Give the extent of all Plasmodium falciparum-infected red blood cells.
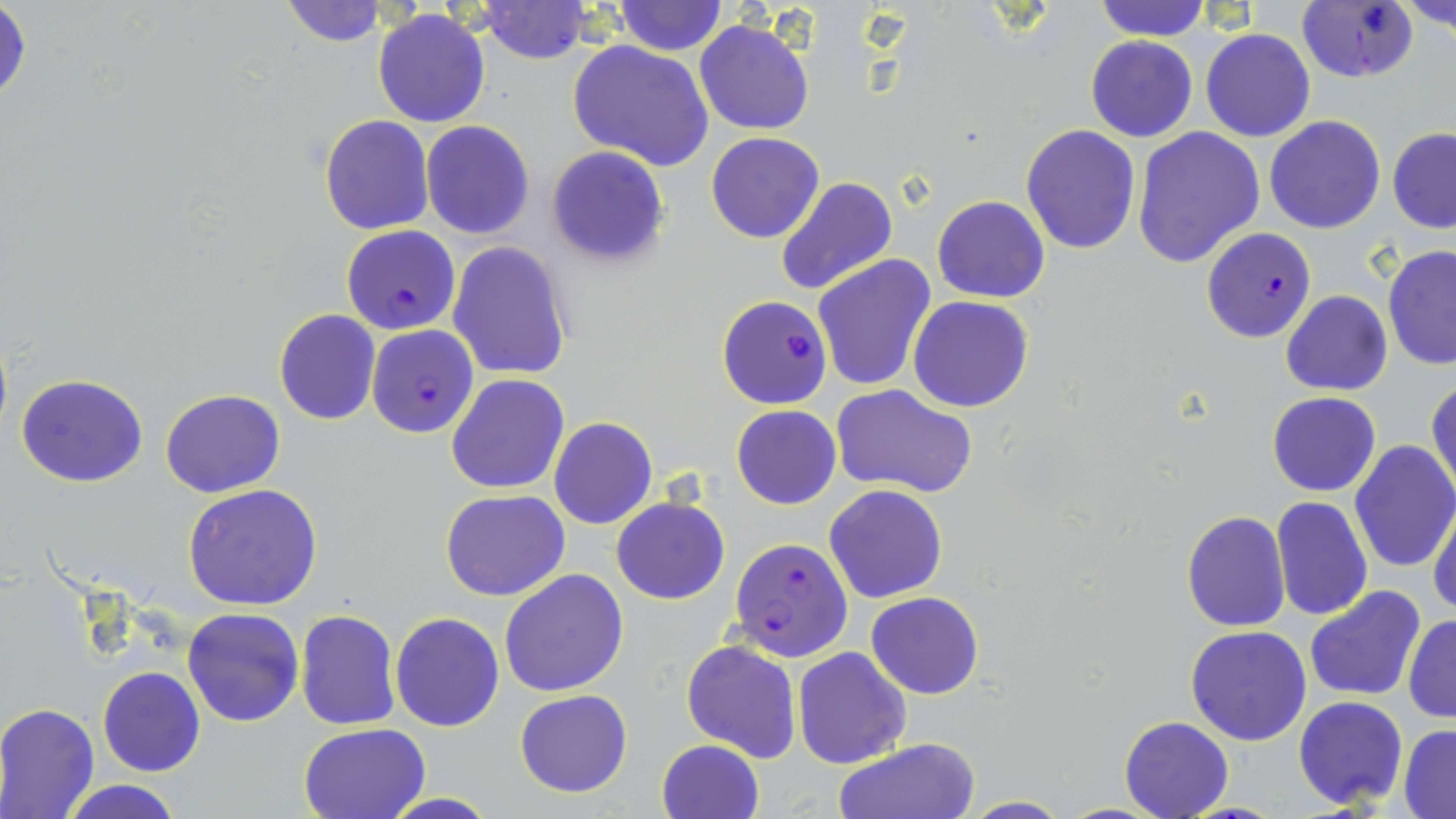
Approximate bounding boxes as named x1/y1/x2/y2 corners in pixels.
Plasmodium falciparum-infected red blood cells: (x1=1294, y1=1, x2=1419, y2=84), (x1=340, y1=225, x2=461, y2=335), (x1=1202, y1=228, x2=1316, y2=343), (x1=716, y1=294, x2=833, y2=410), (x1=367, y1=324, x2=479, y2=439), (x1=730, y1=541, x2=855, y2=673).

slide-level diagnosis = Plasmodium falciparum
stain = May-Grünwald-Giemsa
uninfected red blood cell locations = approximate bounding boxes as named x1/y1/x2/y2 corners in pixels: (x1=280, y1=0, x2=387, y2=47), (x1=613, y1=0, x2=727, y2=55), (x1=1091, y1=0, x2=1212, y2=41), (x1=1398, y1=1, x2=1455, y2=37), (x1=481, y1=2, x2=591, y2=63), (x1=1, y1=3, x2=31, y2=110), (x1=373, y1=10, x2=490, y2=128), (x1=694, y1=20, x2=815, y2=135), (x1=1201, y1=28, x2=1315, y2=140), (x1=1085, y1=36, x2=1198, y2=142), (x1=567, y1=41, x2=714, y2=173), (x1=318, y1=114, x2=435, y2=235), (x1=1263, y1=116, x2=1387, y2=234), (x1=421, y1=120, x2=534, y2=239), (x1=1022, y1=125, x2=1141, y2=253), (x1=1131, y1=127, x2=1264, y2=269), (x1=1387, y1=128, x2=1456, y2=232), (x1=705, y1=131, x2=824, y2=244), (x1=546, y1=146, x2=669, y2=267), (x1=775, y1=176, x2=896, y2=297), (x1=932, y1=195, x2=1049, y2=303), (x1=448, y1=241, x2=573, y2=379), (x1=1382, y1=246, x2=1456, y2=371), (x1=812, y1=254, x2=939, y2=394), (x1=1281, y1=290, x2=1392, y2=396), (x1=908, y1=296, x2=1034, y2=413), (x1=273, y1=309, x2=381, y2=425), (x1=446, y1=373, x2=569, y2=494), (x1=16, y1=374, x2=148, y2=488), (x1=1427, y1=377, x2=1456, y2=497), (x1=829, y1=384, x2=978, y2=498), (x1=160, y1=388, x2=286, y2=498), (x1=1266, y1=392, x2=1381, y2=495), (x1=731, y1=405, x2=841, y2=509), (x1=548, y1=417, x2=659, y2=530), (x1=1350, y1=439, x2=1456, y2=574), (x1=825, y1=484, x2=947, y2=603), (x1=183, y1=485, x2=325, y2=611), (x1=440, y1=489, x2=569, y2=601), (x1=1271, y1=496, x2=1373, y2=621), (x1=610, y1=497, x2=729, y2=604), (x1=1427, y1=502, x2=1456, y2=619), (x1=1182, y1=510, x2=1291, y2=631), (x1=500, y1=569, x2=630, y2=697), (x1=1304, y1=585, x2=1427, y2=702), (x1=866, y1=591, x2=984, y2=700), (x1=183, y1=607, x2=304, y2=728), (x1=296, y1=610, x2=400, y2=730), (x1=389, y1=612, x2=504, y2=731), (x1=1403, y1=614, x2=1455, y2=723), (x1=1185, y1=626, x2=1312, y2=746), (x1=681, y1=638, x2=800, y2=763), (x1=792, y1=647, x2=911, y2=768), (x1=98, y1=667, x2=203, y2=777), (x1=514, y1=688, x2=633, y2=797), (x1=1293, y1=695, x2=1408, y2=809), (x1=0, y1=701, x2=100, y2=818), (x1=1120, y1=715, x2=1233, y2=817), (x1=298, y1=722, x2=431, y2=819), (x1=1399, y1=725, x2=1456, y2=816), (x1=830, y1=737, x2=980, y2=819), (x1=656, y1=738, x2=764, y2=819), (x1=59, y1=780, x2=185, y2=819), (x1=379, y1=793, x2=501, y2=818), (x1=961, y1=797, x2=1074, y2=818)
modality = light microscopy
preparation = thin blood film
field of view = one of a larger specimen
magnification = 1000x
image size = 1456×819 pixels